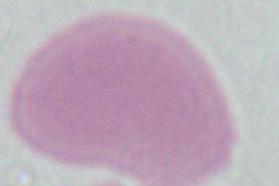

Summary:
  - Magnification: 1000x
  - Modality: micrograph
  - Identification: red blood cell